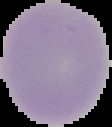

image size = 112×127 pixels
result = no Plasmodium parasites detected
preparation = thin blood smear
image type = cell region segmented out of the field of view; surrounding area masked to black